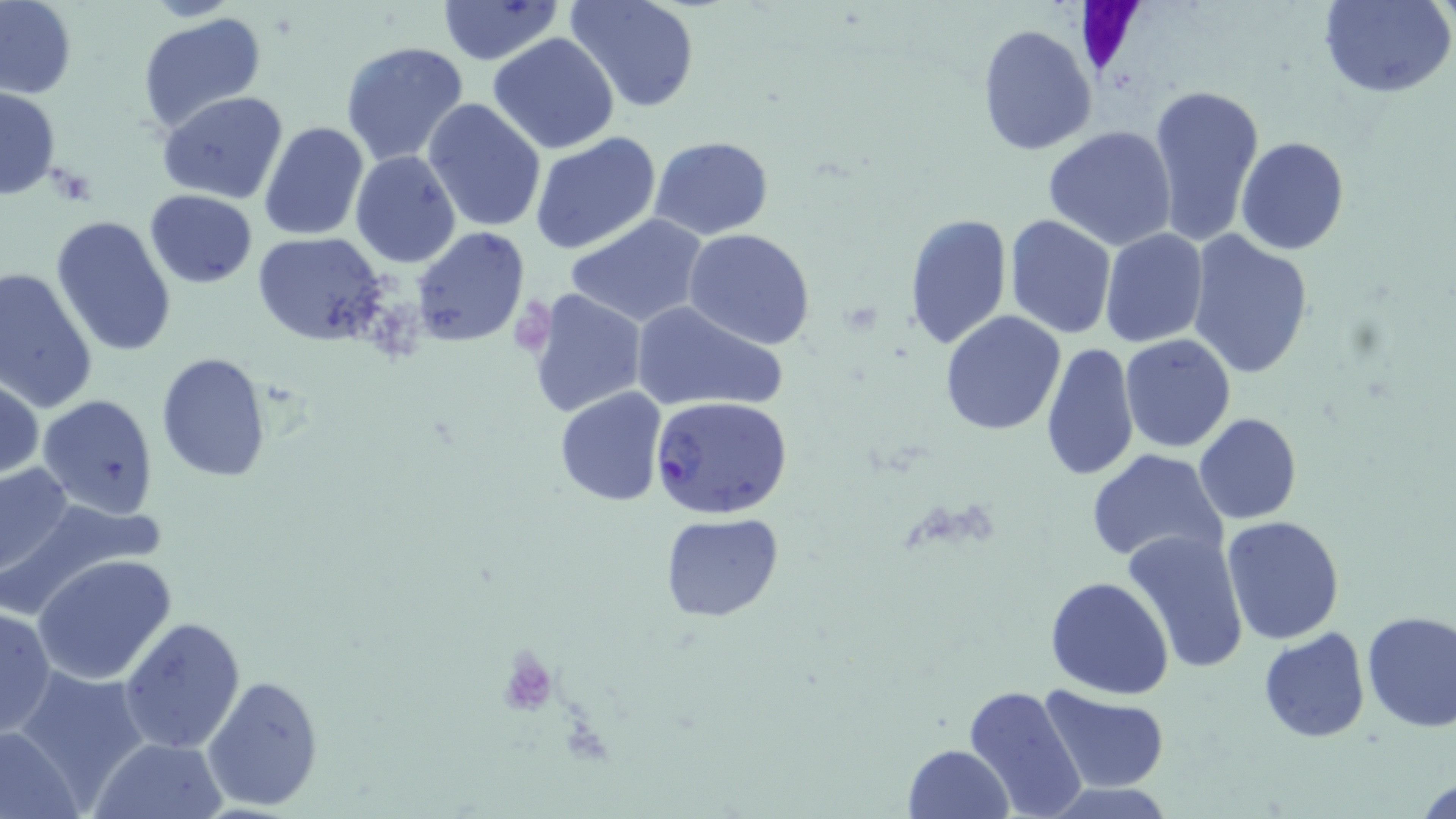 Approximate bounding boxes as [x1, y1, x2, y2] in pixels. Plasmodium falciparum-infected red blood cell locations: [649, 396, 794, 520]. Uninfected red blood cell locations: [0, 0, 77, 100], [437, 0, 564, 65], [565, 0, 701, 114], [1319, 0, 1455, 99], [138, 12, 267, 135], [976, 23, 1097, 157], [487, 34, 621, 154], [340, 42, 471, 168], [1147, 79, 1265, 249], [0, 87, 61, 199], [158, 91, 289, 204], [424, 97, 548, 234], [259, 119, 370, 241], [1042, 125, 1178, 249], [529, 131, 661, 256], [649, 135, 773, 239], [1236, 136, 1350, 255], [351, 150, 461, 269], [144, 189, 258, 288], [901, 212, 1013, 351], [564, 214, 709, 327], [1004, 214, 1117, 339], [51, 215, 179, 360], [411, 227, 528, 348], [684, 229, 816, 350], [1099, 229, 1208, 348], [1186, 231, 1315, 378], [253, 233, 392, 344], [0, 267, 99, 413], [527, 288, 647, 419], [629, 299, 786, 415], [939, 310, 1066, 434], [1119, 334, 1237, 454], [1040, 341, 1140, 482], [154, 353, 272, 482], [1, 374, 42, 482], [555, 386, 669, 509], [36, 394, 158, 519], [1193, 413, 1302, 525], [1084, 450, 1229, 570], [1, 461, 76, 585], [2, 500, 165, 616], [659, 512, 783, 622], [1220, 516, 1345, 644], [1123, 529, 1251, 670], [33, 553, 178, 687], [1045, 575, 1174, 700], [0, 603, 55, 738], [1360, 609, 1456, 732], [117, 616, 247, 755], [1258, 628, 1369, 743], [9, 672, 151, 806], [202, 675, 326, 810], [963, 684, 1090, 819], [1038, 686, 1169, 795], [0, 723, 86, 819], [91, 737, 229, 819], [903, 743, 1013, 818], [1416, 770, 1456, 819]. Slide-level diagnosis: Plasmodium falciparum. 1000x magnification. One field of a larger specimen. Image is 1456×819 pixels. Optical microscopy. May-Grünwald-Giemsa stain. Thin blood film.